Identify the parasite.
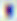
This is Toxoplasma gondii.

400x magnification. Photomicrograph.